Outline each blood parasite and name the species.
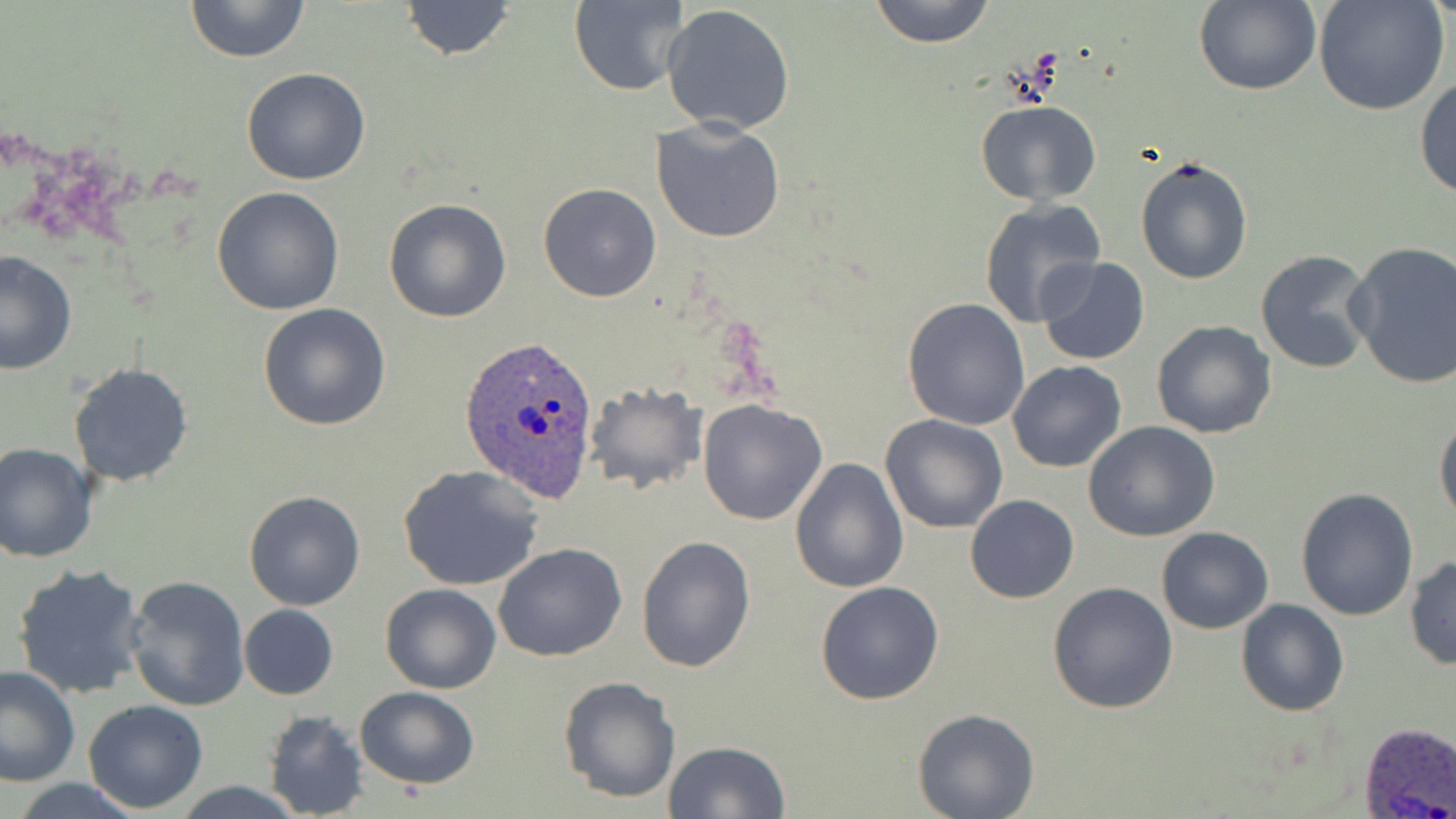

Approximate bounding boxes as (x1,y1)-(x2,y2) corner pairs in pixels.
Plasmodium ovale-infected red blood cells: (460,337)-(598,503), (1358,721)-(1456,819).
No Plasmodium falciparum, Plasmodium malariae, Plasmodium vivax, Babesia divergens, or Trypanosoma brucei observed.

Summary:
  - Uninfected red blood cell locations: (185,0)-(311,65), (569,0)-(690,95), (869,0)-(996,48), (396,1)-(517,60), (1193,1)-(1322,96), (1313,1)-(1449,116), (661,4)-(797,135), (241,66)-(370,185), (1414,75)-(1456,200), (974,99)-(1102,206), (651,118)-(786,243), (1134,156)-(1253,286), (538,182)-(662,301), (211,187)-(344,315), (383,197)-(512,322), (978,198)-(1107,330), (1345,240)-(1456,389), (1255,249)-(1380,375), (0,250)-(76,375), (1037,258)-(1150,367), (903,296)-(1032,431), (257,303)-(391,431), (1150,319)-(1277,438), (1006,360)-(1126,472), (68,363)-(194,486), (584,381)-(708,496), (696,397)-(826,524), (1434,412)-(1456,527), (879,414)-(1007,534), (1083,420)-(1220,541), (1,442)-(97,564), (790,458)-(907,594), (398,465)-(547,593), (1295,487)-(1419,620), (244,490)-(365,611), (966,495)-(1079,604), (1157,526)-(1273,634), (637,533)-(756,673), (492,541)-(627,661), (1405,555)-(1456,669), (10,562)-(150,701), (124,574)-(250,711), (815,581)-(944,703), (1047,581)-(1178,715), (379,583)-(502,694), (1235,599)-(1350,717), (239,604)-(339,700), (0,666)-(78,786), (556,675)-(682,804), (356,686)-(479,789), (82,699)-(208,814), (912,708)-(1039,819), (261,709)-(372,819), (663,741)-(790,819), (172,782)-(308,818)
  - Slide-level diagnosis: Plasmodium ovale
  - Field of view: single
  - Stain: May-Grünwald-Giemsa
  - Image size: 1456×819 pixels
  - Magnification: 1000x
  - Modality: light microscopy
  - Preparation: thin blood smear